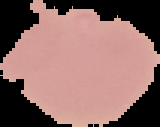
result = no Plasmodium parasites seen
preparation = thin blood film
image size = 160×127 pixels
image type = segmented cell region on a black background